Identify the preparation type.
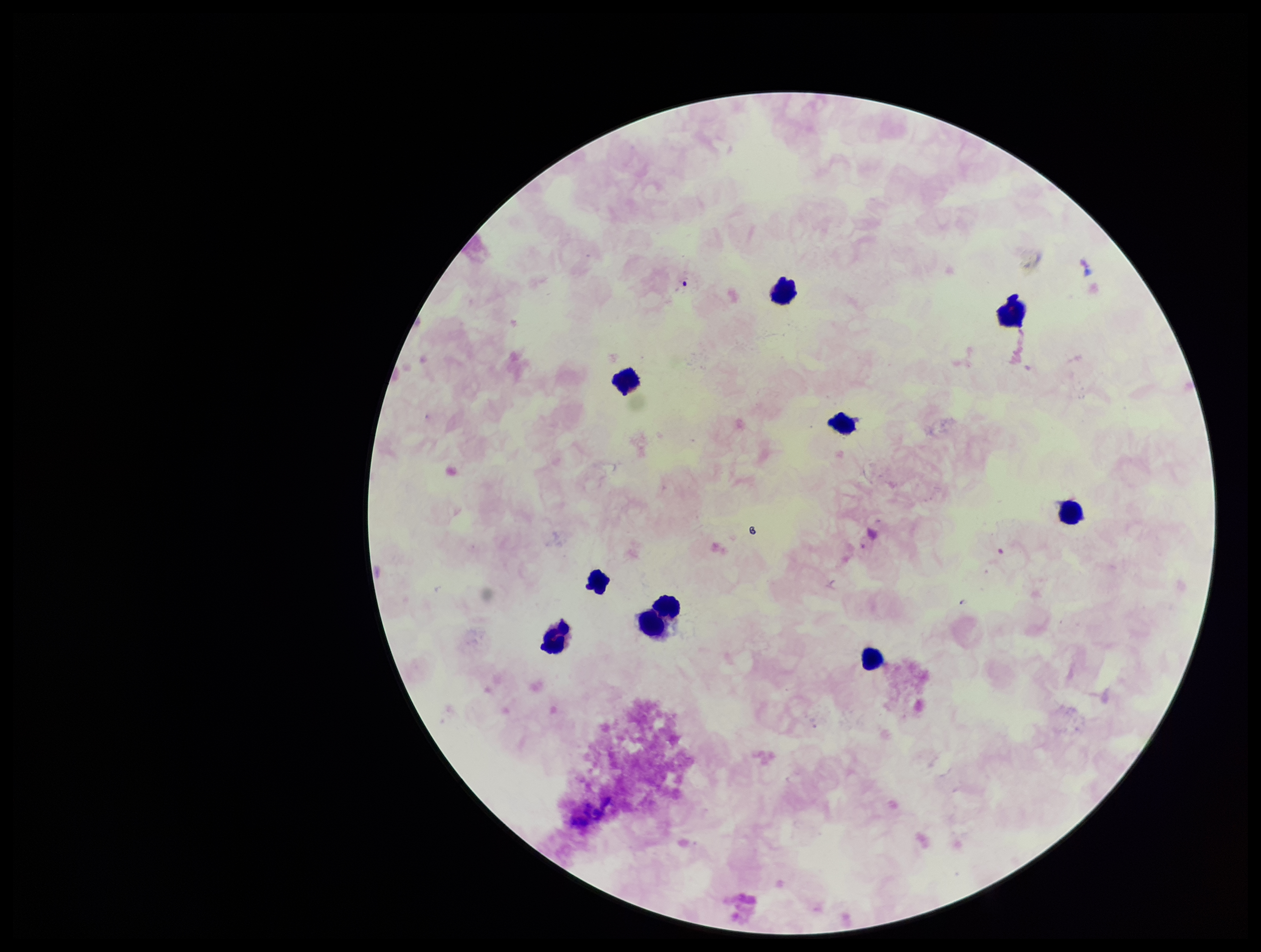
Thick.

parasite count = 0
image size = 1261×952 pixels
stain = Giemsa
leukocyte count = 10
patient malaria status = negative
field of view = one from this slide
Plasmodium parasites = none identified
capture = smartphone photograph through the microscope eyepiece